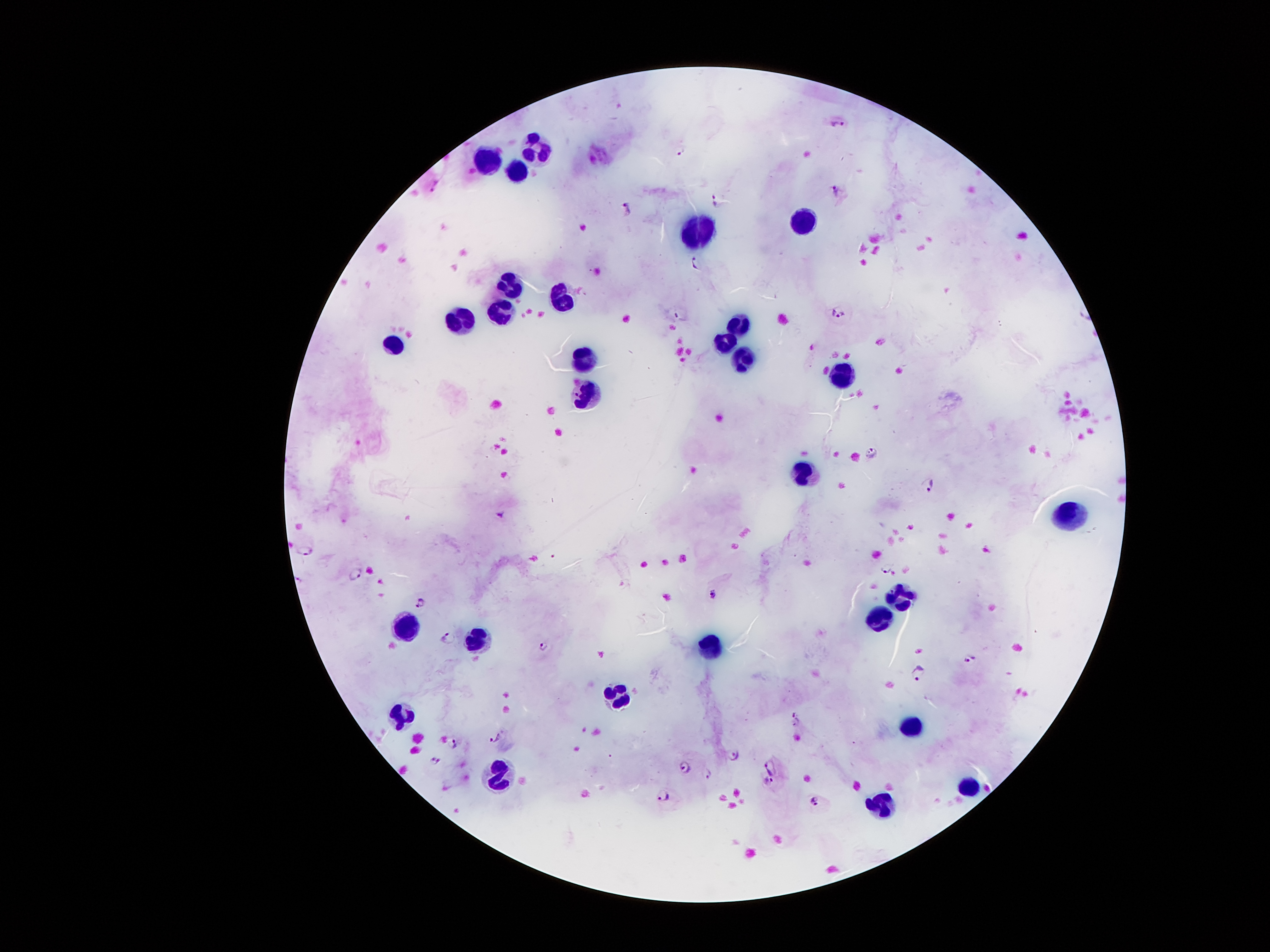
{
  "patient_malaria_status": "positive for Plasmodium falciparum",
  "field_of_view": "single",
  "preparation": "thick peripheral-blood smear",
  "leukocyte_locations": "approximate centers as {x, y} in pixels: {538, 144}, {485, 157}, {513, 171}, {802, 221}, {695, 226}, {510, 279}, {563, 300}, {500, 314}, {449, 319}, {738, 326}, {726, 340}, {394, 347}, {585, 352}, {743, 361}, {846, 370}, {580, 395}, {805, 471}, {1069, 516}, {901, 592}, {882, 615}, {409, 624}, {476, 640}, {711, 651}, {616, 698}, {400, 714}, {915, 727}, {497, 770}, {969, 782}, {881, 805}",
  "magnification": "100x",
  "capture": "smartphone camera through the microscope eyepiece",
  "stain": "Giemsa",
  "image_size": "1270×952 pixels",
  "plasmodium_parasite_locations": "approximate centers as {x, y} in pixels: {837, 124}, {681, 150}, {436, 183}, {837, 189}, {718, 200}, {627, 210}, {695, 264}, {838, 313}, {681, 315}, {871, 451}, {928, 484}, {501, 514}, {307, 551}, {886, 568}, {355, 573}, {714, 593}, {420, 602}, {449, 636}, {543, 645}, {970, 659}, {918, 671}, {797, 717}, {493, 736}, {452, 743}, {734, 754}, {434, 761}, {768, 763}, {682, 764}, {708, 771}, {769, 783}, {662, 795}, {814, 800}"
}